Identify the parasite.
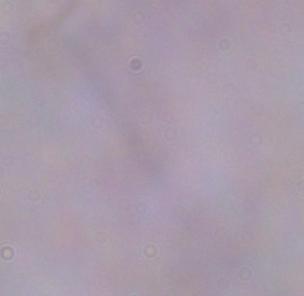
A trypanosome.

modality = photomicrograph
magnification = 1000x